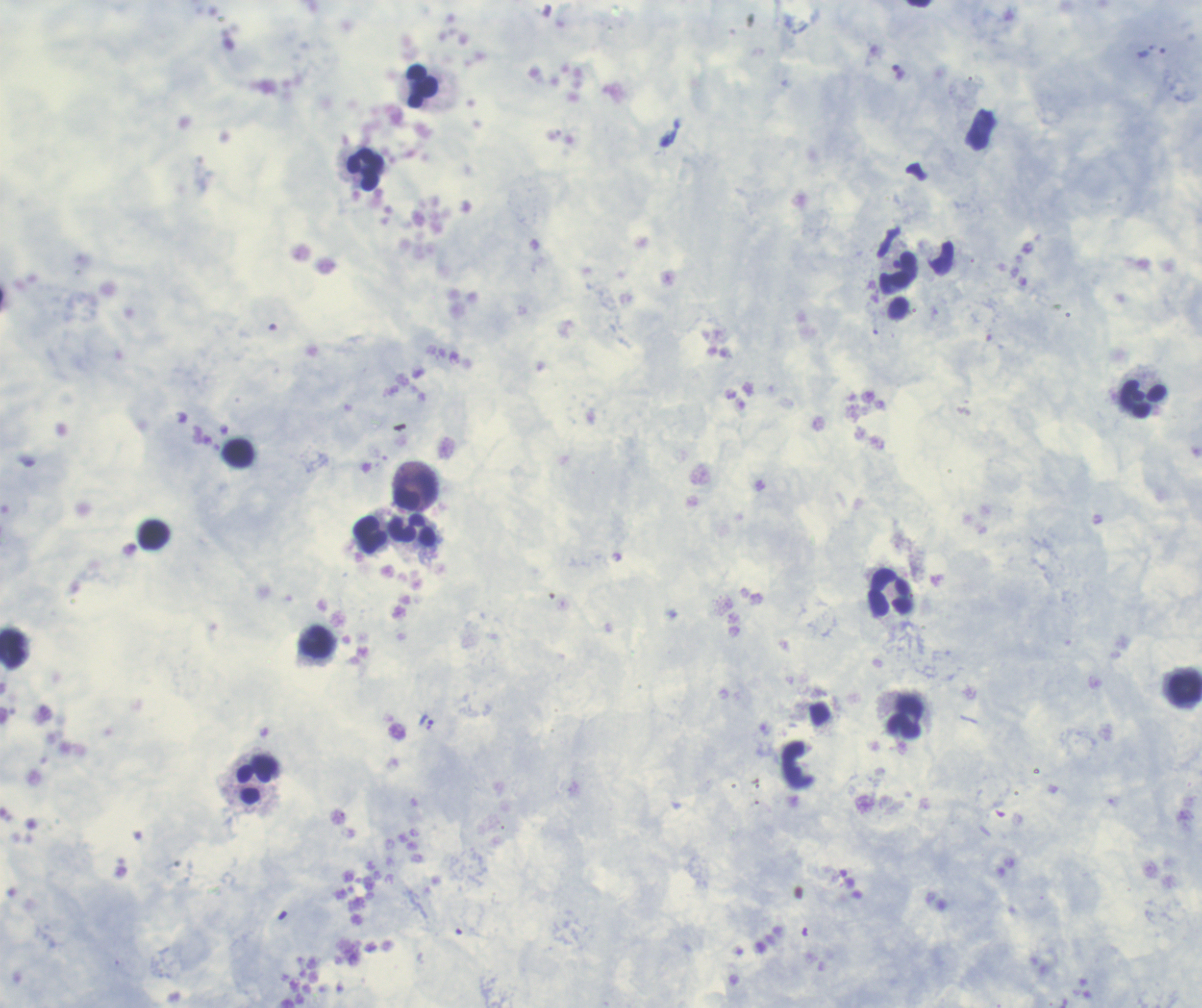

Approximate centers as {x, y} in pixels. Trophozoite locations: {426, 721}. Leukocyte locations: {422, 85}, {365, 170}, {898, 273}, {1142, 399}, {238, 452}, {415, 491}, {413, 530}, {369, 534}, {153, 535}, {890, 591}, {317, 642}, {12, 649}, {1185, 688}, {904, 717}, {253, 783}. Result: malaria parasites identified. One field from this slide. Coloration quality: good. Previously used in a real diagnosis. Thick blood smear. Image is 1202×1008 pixels. 100x magnification. Background quality: good. Romanowsky stain.